Locate every Plasmodium parasite.
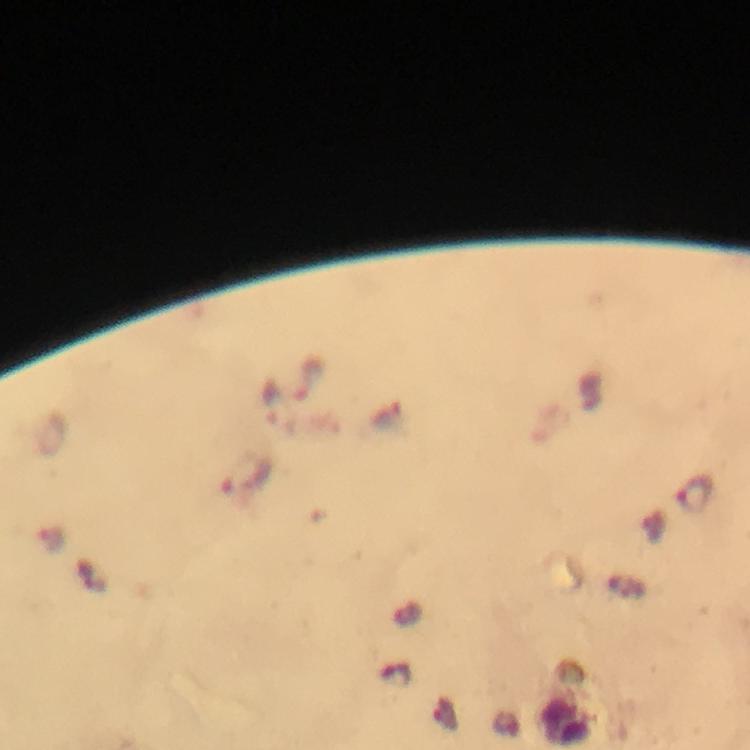
Approximate centers as [x, y] in pixels.
Plasmodium parasites: [246, 476], [693, 493].

Summary:
  - Context: from a diagnostic examination for malaria
  - Cropped from: a single field of view
  - Image size: 750×750 pixels
  - Preparation: thick blood smear
  - Magnification: 100x
  - Capture: smartphone photograph through a microscope
  - Stain: Giemsa
  - Immersion oil: applied